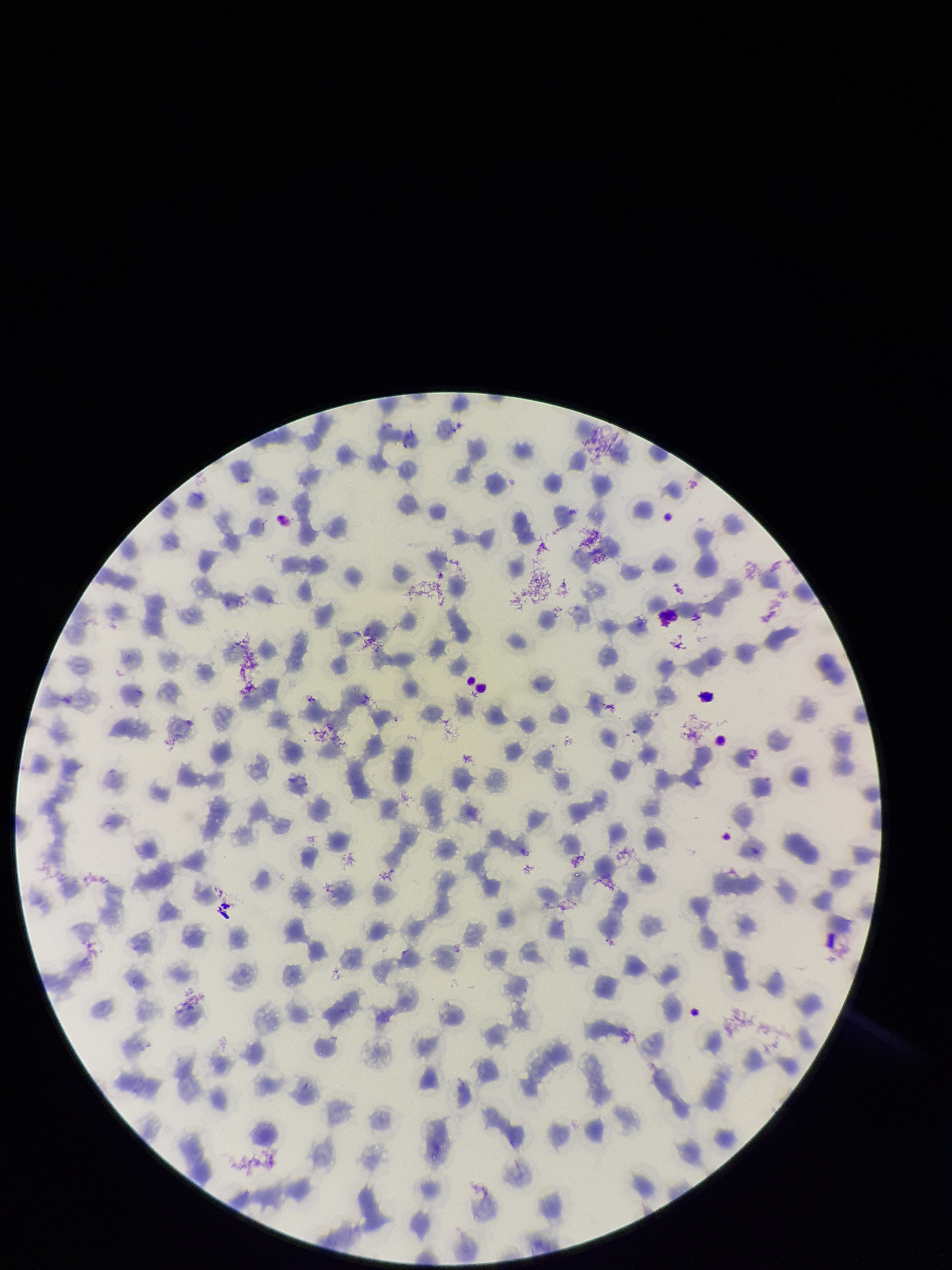 Photographed through the microscope eyepiece with a smartphone camera. Preparation: thin. Red blood cell count: 138. Parasitized red blood cells: none detected. Giemsa stain. Patient malaria status: infected. Species reported for this patient: Plasmodium falciparum. One field from this slide. Image is 952×1270 pixels. Parasitized red blood cell count: 0.